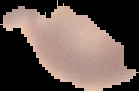
preparation = thin blood smear
image type = segmented cell region with the area outside set to black
image size = 139×91 pixels
malaria status = uninfected